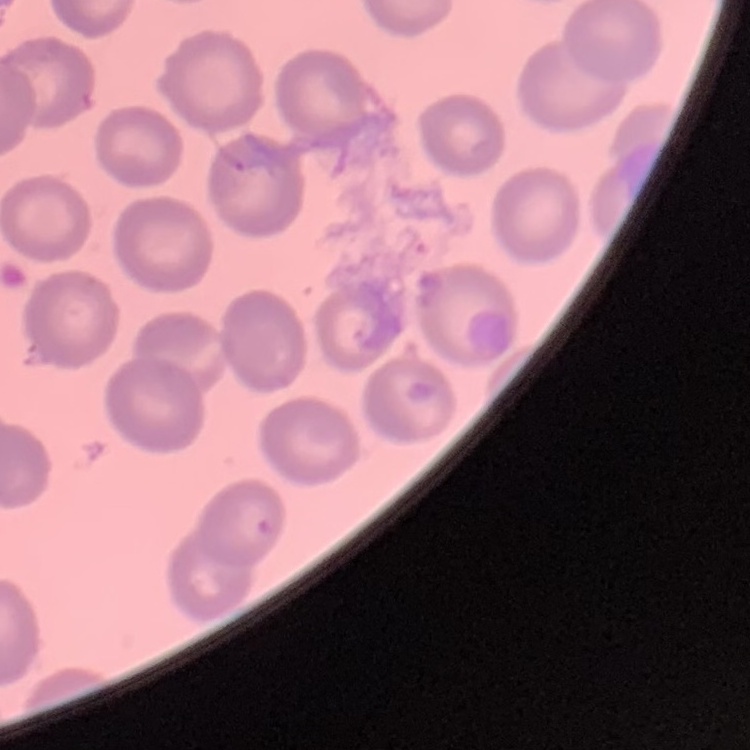

Summary:
  - Red blood cell morphology: no rouleaux formation
  - Image type: square crop of a larger photomicrograph
  - Preparation: thin peripheral smear
  - Stain: Field's or Giemsa